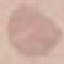

malaria status = uninfected
preparation = thin blood film
capture = smartphone through the microscope eyepiece
image type = automatically extracted cell patch, resized to 64 × 64 pixels
stain = Giemsa